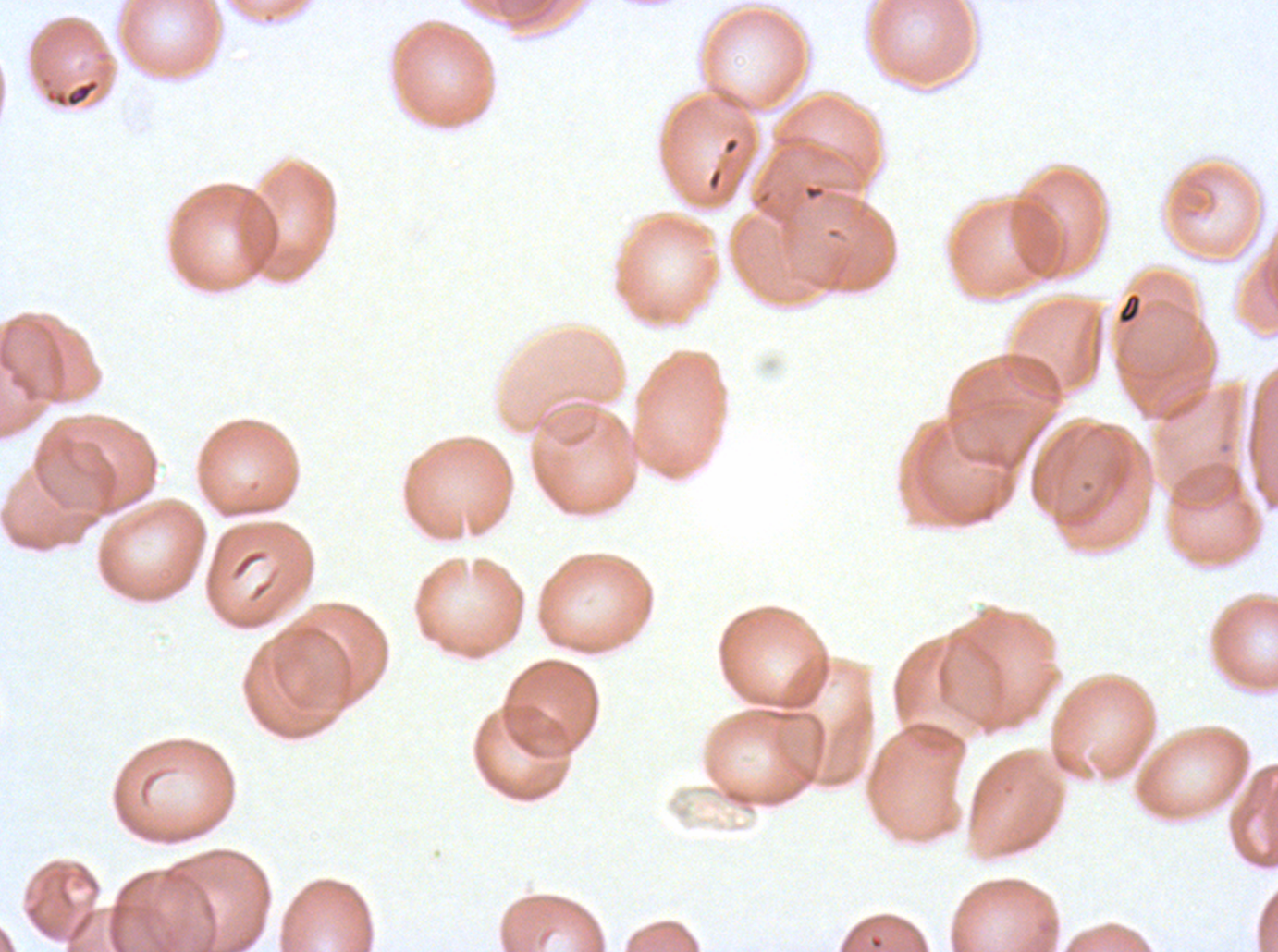

image_size: 1278×952 pixels
preparation: thin blood film
field_of_view: one sub-image of a larger composite
specimen: ex-vivo Plasmodium falciparum culture from a patient in The Gambia, grown for 24 to 48 hours
stain: Giemsa
debris_locations: 'approximate bounding rectangles given as corner coordinates in pixels from the top-left: (x1=40, y1=75, x2=102, y2=109), (x1=803, y1=183, x2=826, y2=201), (x1=1117, y1=292, x2=1142, y2=324)'